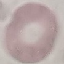
malaria status = uninfected
image type = automatically extracted cell patch, resized to 64 × 64 pixels
capture = smartphone through the microscope eyepiece
preparation = thin blood smear
stain = Giemsa